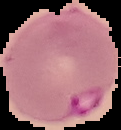
Summary:
  - Image type: cell region segmented out of the field of view; surrounding area masked to black
  - Preparation: thin blood film
  - Image size: 121×130 pixels
  - Result: malaria parasites identified